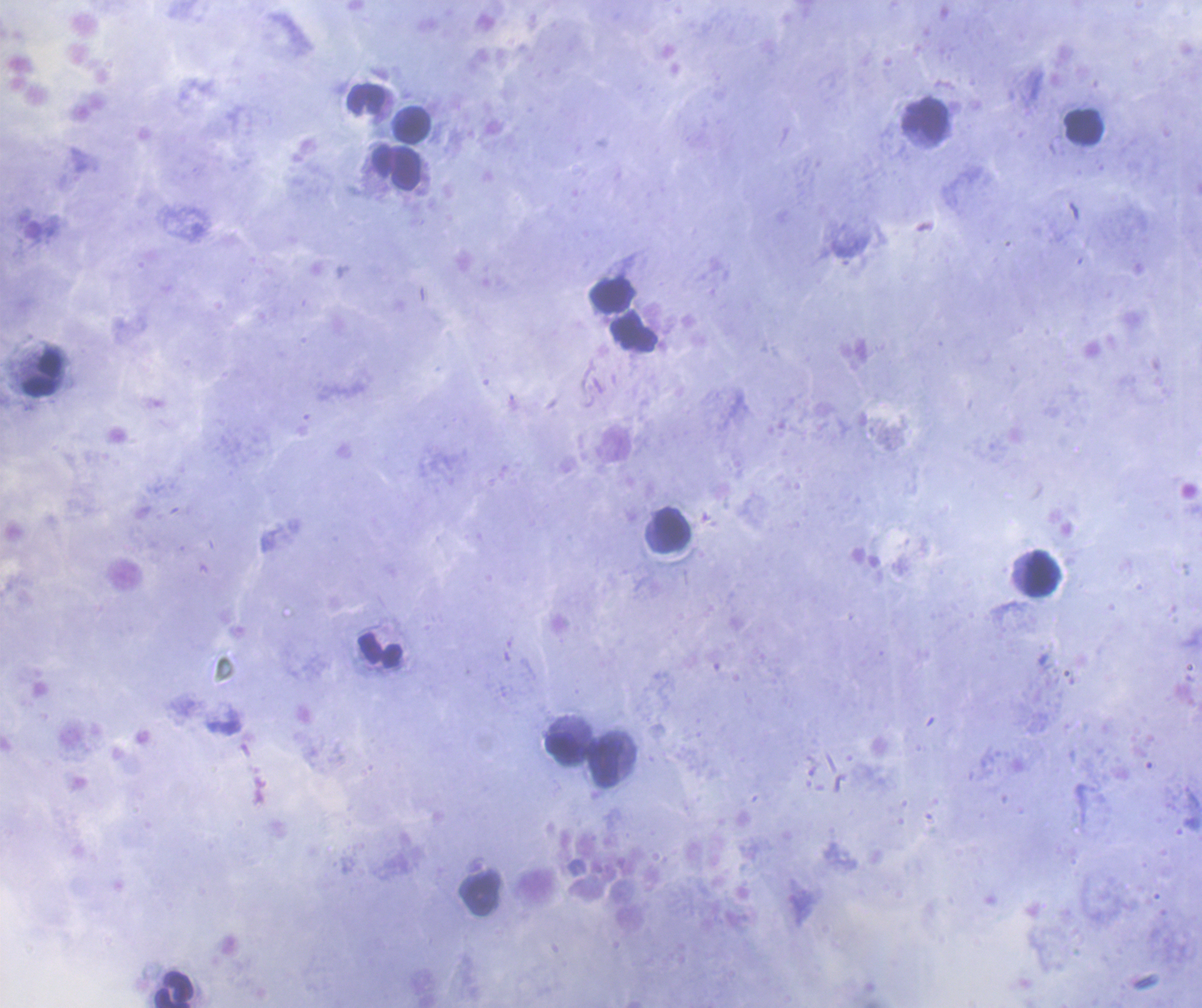
Approximate centers as {x, y} in pixels.
Summary:
  - Leukocyte locations: {367, 99}, {926, 121}, {412, 126}, {1084, 128}, {397, 167}, {613, 296}, {634, 331}, {43, 374}, {672, 529}, {1042, 574}, {380, 649}, {566, 747}, {607, 760}, {479, 896}, {174, 989}
  - Background quality: satisfactory
  - Preparation: thick blood smear
  - Context: previously used in a real diagnosis
  - Stain: Romanowsky
  - Coloration quality: good
  - Field of view: single
  - Magnification: 100x
  - Result: no malaria parasites seen
  - Image size: 1202×1008 pixels